Report the malaria status of this cell.
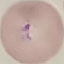
It is parasitized.

image_type: cell patch, automatically extracted from a larger field of view and resized to 64 × 64 pixels
stain: Giemsa
preparation: thin blood smear
capture: smartphone through the microscope eyepiece